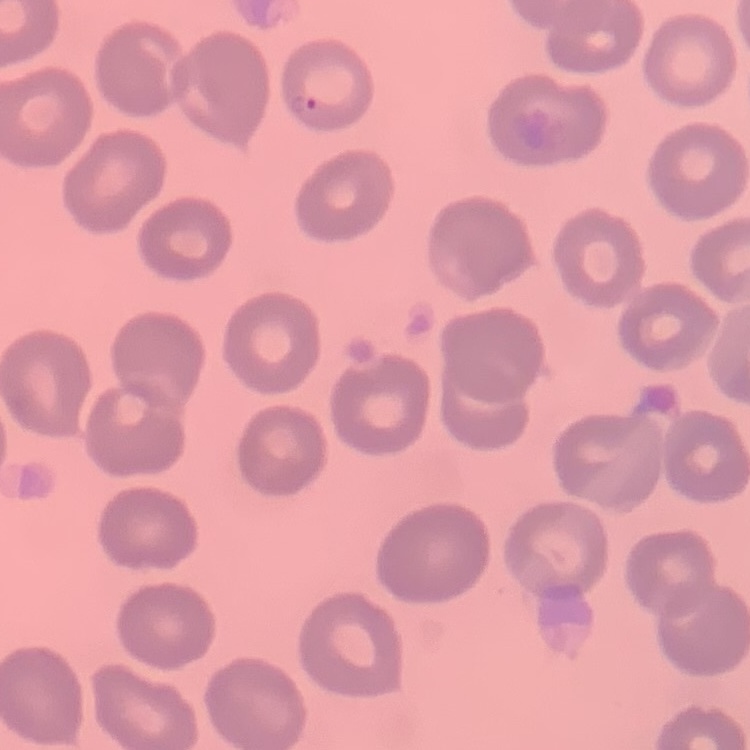

red_blood_cell_morphology: no rouleaux formation
preparation: thin blood film
stain: Field's or Giemsa
image_type: square crop of a larger photomicrograph